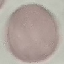
Summary:
  - Malaria status: uninfected
  - Stain: Giemsa
  - Capture: smartphone through the microscope eyepiece
  - Image type: cell patch, automatically extracted from a larger field of view and resized to 64 × 64 pixels
  - Preparation: thin smear